Outline each blood parasite and name the species.
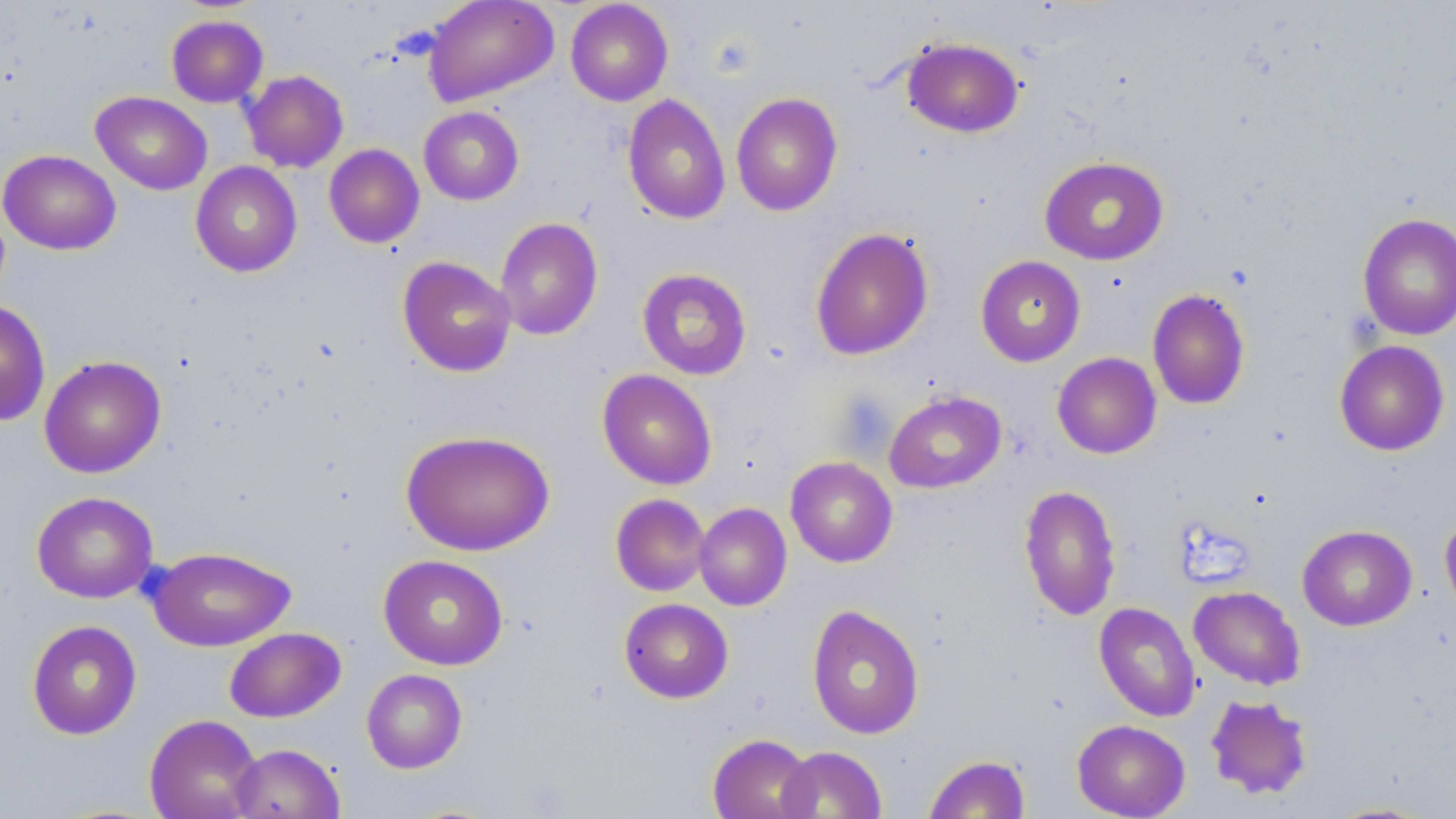

No blood parasites seen.

Summary:
  - Coordinate format: approximate bounding boxes as [x1, y1, x2, y2] in pixels
  - Uninfected red blood cell locations: [423, 0, 559, 106], [565, 1, 673, 106], [166, 15, 268, 107], [900, 35, 1025, 138], [242, 70, 349, 173], [91, 91, 212, 195], [731, 92, 843, 216], [622, 93, 731, 225], [418, 106, 524, 205], [324, 144, 425, 248], [0, 149, 121, 255], [1039, 155, 1169, 265], [190, 161, 302, 277], [1357, 212, 1456, 340], [494, 216, 603, 341], [810, 227, 933, 360], [975, 255, 1086, 366], [397, 256, 516, 377], [637, 268, 752, 380], [1147, 288, 1250, 409], [0, 298, 50, 426], [1334, 340, 1450, 456], [1052, 352, 1162, 458], [39, 355, 166, 478], [597, 369, 717, 490], [883, 390, 1006, 493], [400, 429, 555, 556], [785, 456, 898, 567], [1018, 484, 1121, 621], [32, 491, 158, 603], [610, 493, 711, 596], [694, 502, 792, 611], [1440, 512, 1456, 626], [1297, 524, 1417, 631], [147, 545, 296, 652], [378, 554, 508, 670], [1188, 585, 1306, 689], [619, 598, 733, 703], [1094, 602, 1200, 722], [806, 603, 925, 740], [26, 620, 142, 740], [225, 627, 346, 722], [361, 668, 468, 773], [1205, 694, 1313, 800], [144, 714, 263, 819], [1072, 719, 1190, 818], [708, 733, 816, 819], [230, 743, 344, 819], [778, 746, 887, 818], [923, 754, 1031, 818], [1323, 801, 1440, 818]
  - Slide-level diagnosis: no evidence of blood parasites
  - Stain: May-Grünwald-Giemsa
  - Magnification: 1000x
  - Field of view: one of a larger specimen
  - Modality: light microscopy
  - Preparation: thin blood film
  - Image size: 1456×819 pixels